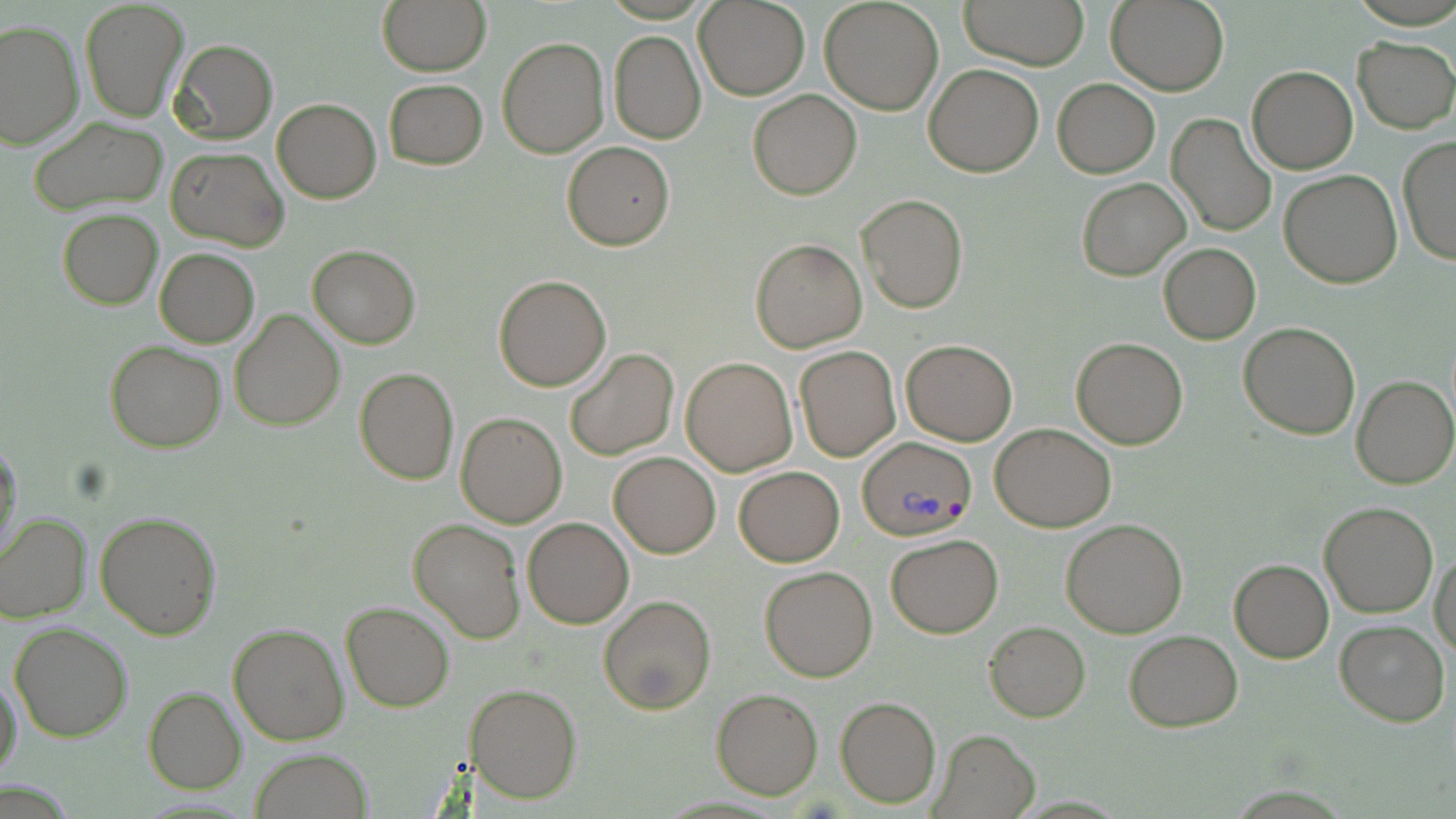

Summary:
  - Coordinate format: approximate bounding boxes as (x1,y1)-(x2,y2) corner pairs in pixels
  - Plasmodium vivax-infected red blood cell locations: (860,438)-(977,542)
  - Uninfected red blood cell locations: (376,0)-(491,76), (820,0)-(944,116), (959,0)-(1091,70), (1106,0)-(1229,95), (79,1)-(188,123), (694,1)-(809,100), (0,21)-(84,151), (608,30)-(706,144), (1352,36)-(1455,132), (497,37)-(609,157), (169,38)-(278,145), (924,63)-(1043,177), (1246,66)-(1358,174), (1053,77)-(1160,177), (385,78)-(488,169), (748,90)-(861,200), (271,98)-(381,204), (1166,113)-(1277,237), (27,117)-(168,214), (1398,138)-(1455,264), (562,140)-(676,251), (165,146)-(289,251), (1279,170)-(1403,290), (1076,177)-(1190,281), (856,193)-(969,315), (58,209)-(163,310), (751,238)-(866,352), (1158,244)-(1259,345), (307,245)-(421,348), (155,249)-(259,348), (494,274)-(612,391), (229,308)-(344,430), (1239,322)-(1361,439), (1070,337)-(1187,449), (900,339)-(1017,446), (105,341)-(227,452), (795,346)-(900,461), (565,348)-(679,462), (681,357)-(797,476), (354,367)-(458,484), (1351,375)-(1456,488), (457,412)-(568,527), (989,423)-(1115,532), (0,437)-(23,562), (608,453)-(720,558), (733,467)-(844,567), (1319,501)-(1439,618), (94,511)-(222,640), (1,512)-(91,622), (523,516)-(634,628), (408,519)-(526,643), (1060,519)-(1189,638), (884,534)-(1002,638), (1430,550)-(1456,661), (1229,559)-(1333,663), (759,565)-(878,682), (600,595)-(716,715), (341,601)-(453,712), (1335,618)-(1449,727), (984,621)-(1091,721), (9,623)-(132,742), (226,623)-(348,746), (1124,629)-(1242,732), (0,672)-(23,782), (467,682)-(582,804), (144,687)-(246,795), (711,688)-(823,800), (834,696)-(940,808), (929,729)-(1038,817), (250,748)-(373,819)
  - Slide-level diagnosis: Plasmodium vivax
  - Image size: 1456×819 pixels
  - Modality: light microscopy
  - Preparation: thin blood smear
  - Stain: May-Grünwald-Giemsa
  - Magnification: 1000x
  - Field of view: one of a larger specimen